Classify this cell by malaria status.
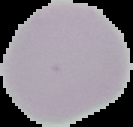
Uninfected.

From a thin blood smear. Cell region segmented out of the field of view; the surrounding area is masked to black. Image is 133×127 pixels.